Locate and identify every blood parasite.
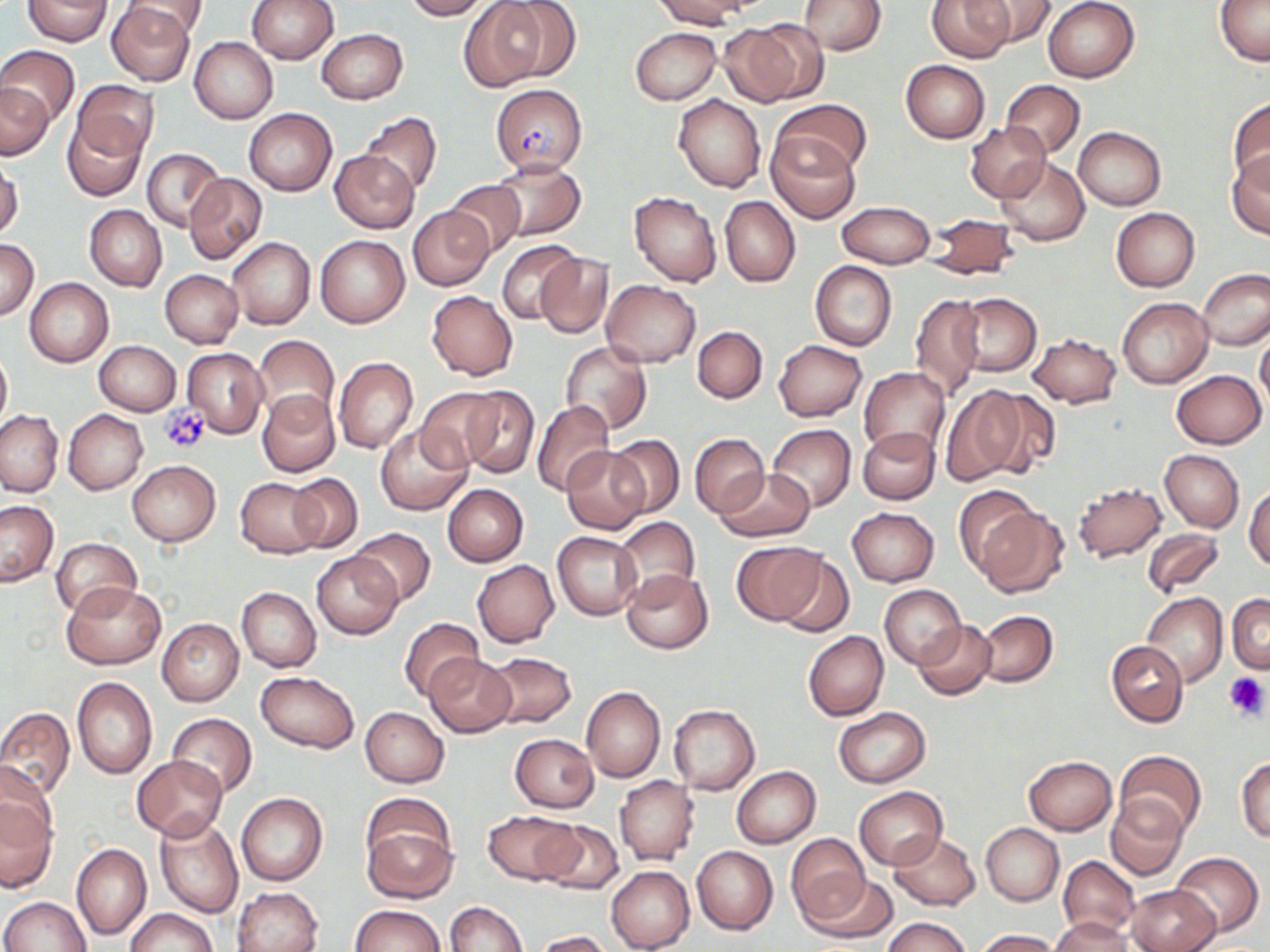
Approximate bounding boxes as (x1, y1, x2, y2) in pixels.
Plasmodium falciparum-infected red blood cells: (491, 84, 587, 175).
No Plasmodium ovale, Plasmodium malariae, Plasmodium vivax, Babesia divergens, or Trypanosoma brucei observed.

{
  "slide_level_diagnosis": "Plasmodium falciparum",
  "image_size": "1270×952 pixels",
  "preparation": "thin blood film",
  "modality": "optical microscopy",
  "stain": "May-Grünwald-Giemsa",
  "platelet_locations": "approximate bounding boxes as (x1, y1, x2, y2) in pixels: (159, 402, 213, 454), (1223, 672, 1269, 720)",
  "field_of_view": "one of a larger specimen",
  "uninfected_red_blood_cell_locations": "approximate bounding boxes as (x1, y1, x2, y2) in pixels: (125, 0, 209, 38), (247, 0, 338, 64), (404, 0, 490, 20), (494, 0, 582, 82), (653, 0, 751, 29), (928, 0, 1012, 62), (973, 0, 1056, 46), (1043, 0, 1140, 82), (1215, 0, 1270, 67), (23, 1, 114, 46), (458, 1, 548, 93), (798, 1, 887, 55), (106, 2, 198, 85), (727, 21, 825, 104), (630, 27, 721, 105), (316, 28, 407, 103), (190, 37, 278, 124), (0, 45, 80, 126), (900, 59, 991, 143), (73, 80, 159, 159), (1001, 80, 1085, 158), (0, 82, 54, 159), (673, 92, 766, 193), (1228, 96, 1270, 188), (773, 99, 870, 179), (244, 108, 336, 196), (358, 111, 442, 196), (62, 114, 145, 201), (963, 121, 1049, 202), (1073, 126, 1166, 210), (766, 130, 862, 224), (141, 149, 225, 230), (329, 149, 420, 233), (1225, 149, 1270, 239), (995, 155, 1090, 246), (489, 157, 584, 240), (1, 159, 23, 240), (183, 173, 267, 264), (443, 181, 527, 257), (629, 191, 721, 287), (720, 196, 800, 287), (839, 201, 933, 268), (84, 205, 167, 291), (408, 206, 492, 291), (1110, 208, 1199, 292), (925, 213, 1020, 280), (314, 235, 409, 328), (227, 237, 316, 329), (1, 240, 38, 319), (497, 240, 584, 325), (535, 254, 613, 338), (810, 261, 897, 351), (1196, 268, 1270, 352), (160, 269, 242, 347), (24, 278, 112, 366), (601, 279, 702, 367), (427, 290, 517, 380), (957, 292, 1041, 376), (909, 294, 983, 401), (1117, 297, 1212, 389), (693, 325, 767, 403), (1254, 329, 1270, 413), (1028, 332, 1121, 408), (253, 336, 340, 425), (94, 340, 180, 415), (774, 340, 867, 421), (561, 342, 651, 434), (0, 347, 11, 433), (183, 347, 268, 437), (333, 357, 419, 454), (859, 367, 949, 456), (1171, 370, 1265, 449), (458, 385, 539, 478), (941, 386, 1032, 485), (415, 387, 507, 473), (976, 388, 1061, 478), (257, 389, 340, 477), (532, 400, 615, 496), (0, 409, 64, 497), (63, 409, 148, 493), (375, 424, 471, 516), (767, 424, 856, 512), (858, 427, 940, 505), (690, 433, 769, 518), (605, 435, 685, 518), (563, 447, 647, 533), (1160, 450, 1244, 531), (126, 460, 221, 546), (713, 469, 814, 542), (287, 472, 363, 553), (235, 477, 323, 557), (1071, 482, 1168, 563), (443, 484, 528, 567), (1245, 484, 1270, 571), (955, 485, 1041, 579), (0, 501, 59, 586), (972, 504, 1069, 598), (847, 507, 939, 586), (615, 516, 700, 599), (349, 527, 436, 606), (1142, 527, 1224, 597), (553, 531, 643, 620), (52, 536, 142, 619), (732, 541, 825, 624), (312, 552, 402, 639), (776, 552, 855, 638), (471, 559, 560, 647), (623, 568, 713, 653), (63, 581, 166, 669), (880, 585, 966, 668), (236, 587, 321, 672), (1142, 592, 1228, 687), (1227, 594, 1270, 674), (976, 610, 1057, 687), (400, 617, 483, 701), (156, 618, 244, 706), (913, 620, 996, 698), (803, 631, 888, 720), (1107, 641, 1187, 726), (484, 652, 577, 729), (492, 652, 584, 803), (425, 654, 518, 737), (256, 671, 358, 752), (73, 677, 157, 779), (581, 685, 664, 783), (668, 704, 759, 795), (359, 707, 449, 788), (0, 708, 75, 798), (833, 708, 931, 787), (166, 713, 258, 798), (510, 733, 599, 812), (1115, 750, 1206, 838), (131, 755, 228, 839), (1022, 755, 1116, 836), (1236, 756, 1270, 844), (0, 761, 57, 851), (732, 766, 821, 848), (615, 775, 700, 866), (855, 787, 947, 869), (0, 793, 58, 893), (237, 793, 328, 886), (1107, 796, 1187, 881), (484, 809, 579, 886), (361, 813, 458, 904), (155, 815, 243, 917), (536, 819, 624, 895), (980, 822, 1064, 905), (887, 831, 981, 910), (787, 834, 871, 925), (72, 843, 151, 941), (692, 845, 777, 934), (1168, 851, 1264, 937), (1059, 855, 1139, 942), (606, 866, 695, 952), (807, 871, 900, 945), (1126, 883, 1220, 952), (232, 887, 322, 952), (0, 897, 90, 951), (444, 901, 527, 952), (349, 904, 445, 952), (125, 908, 216, 952), (882, 916, 970, 952), (1053, 916, 1134, 952), (976, 929, 1061, 952), (533, 930, 616, 951)",
  "magnification": "1000x"
}